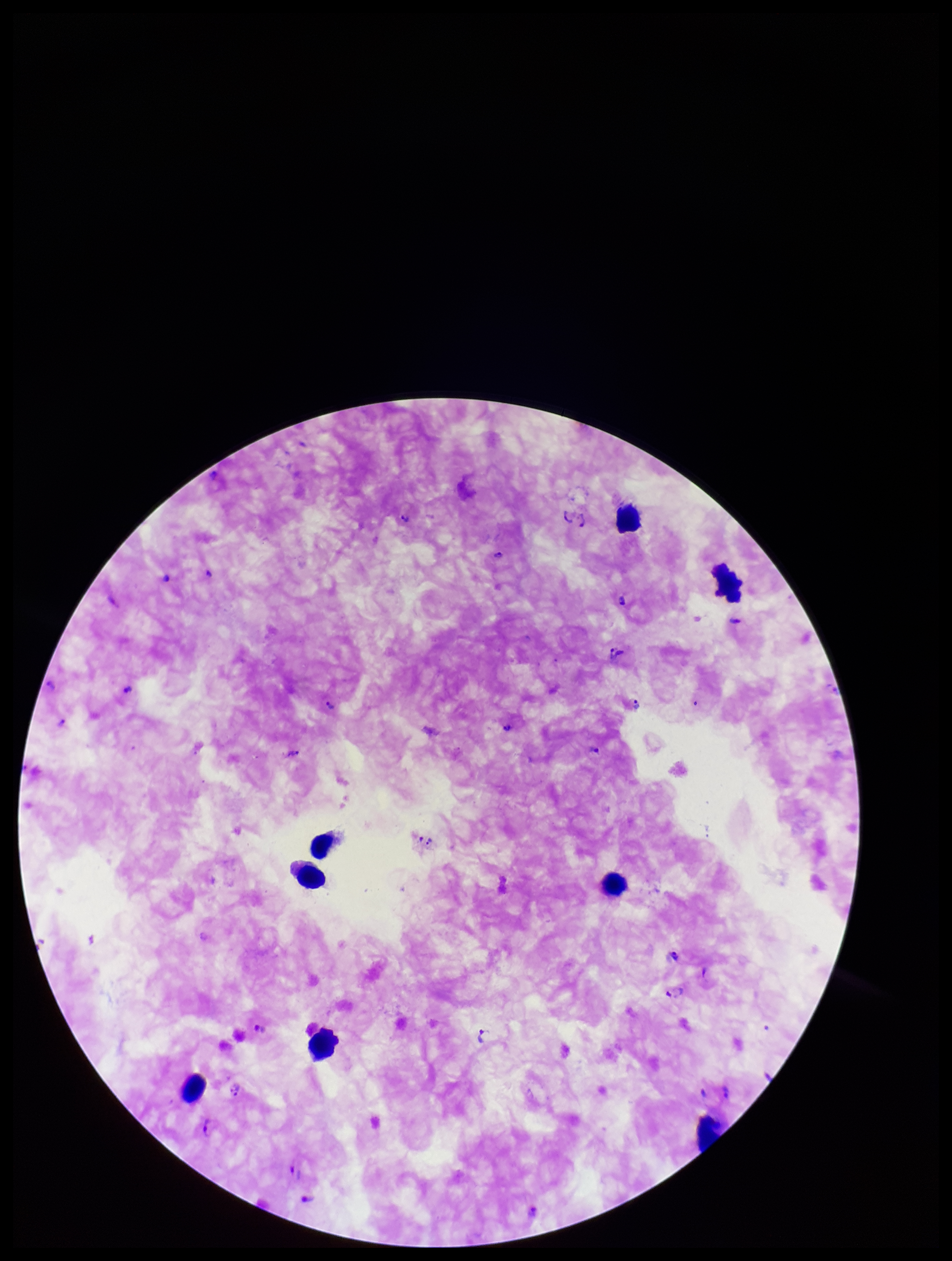

Giemsa stain. Single field of view. Parasite count: 21. Plasmodium parasites: seen. Photographed through the microscope eyepiece with a smartphone camera. Image is 952×1261 pixels. Leukocyte count: 8. Patient malaria status: infected. Preparation: thick. Species reported for this patient: Plasmodium falciparum.